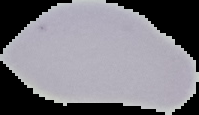 Image is 199×115 pixels. From a thin blood smear. The area outside the segmented cell region is set to black. Malaria status: uninfected.